Assess this cell for malaria.
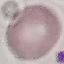
Uninfected.

image type = automatically extracted cell patch, resized to 64 × 64 pixels
capture = smartphone camera at the microscope eyepiece
preparation = thin blood smear
stain = Giemsa